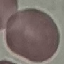

result: no malaria parasites seen
capture: smartphone camera at the microscope eyepiece
preparation: thin blood smear
image_type: automatically extracted cell patch, resized to 64 × 64 pixels
stain: Giemsa